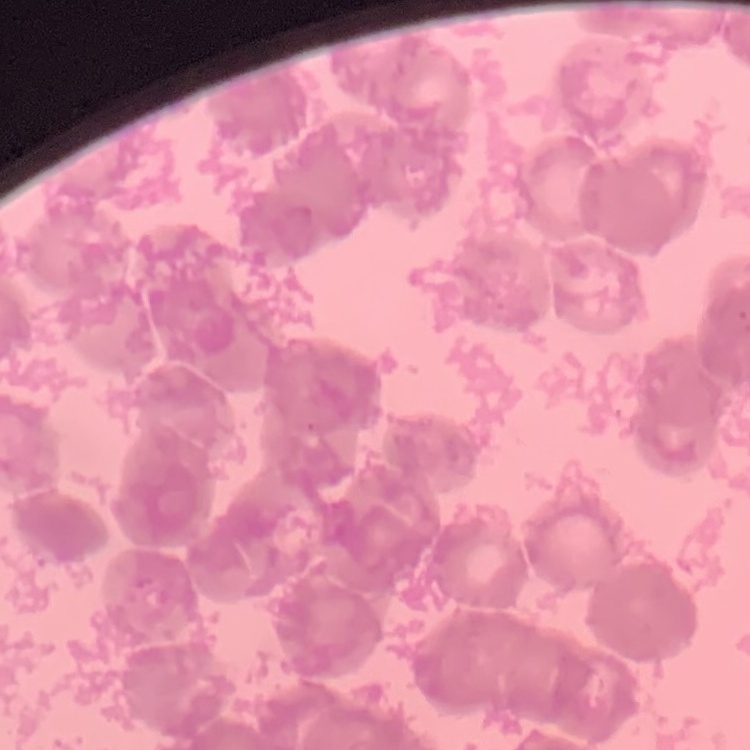

{
  "red_blood_cell_morphology": "rouleaux formation",
  "image_type": "one tile cut from a larger photomicrograph",
  "stain": "Field's or Giemsa",
  "preparation": "thin blood film"
}